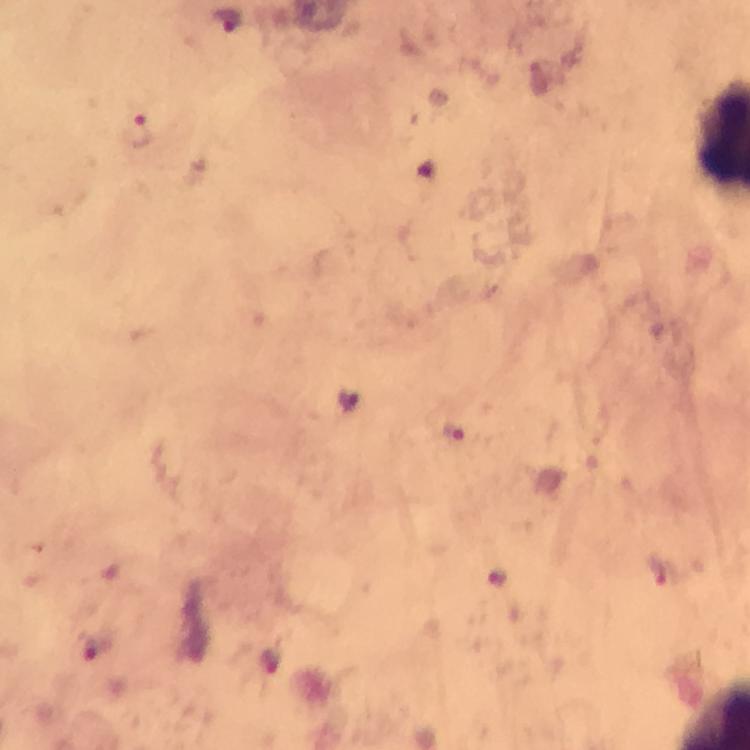

stain: Giemsa
context: from a malaria diagnostic workup
immersion_oil: applied
malaria_parasite_locations: 'approximate centers as (x, y) in pixels: (226, 20), (137, 133), (452, 432), (659, 572), (93, 649), (271, 660)'
cropped_from: one field of view
image_size: 750×750 pixels
magnification: 100x
capture: smartphone photograph through a microscope
preparation: thick blood smear